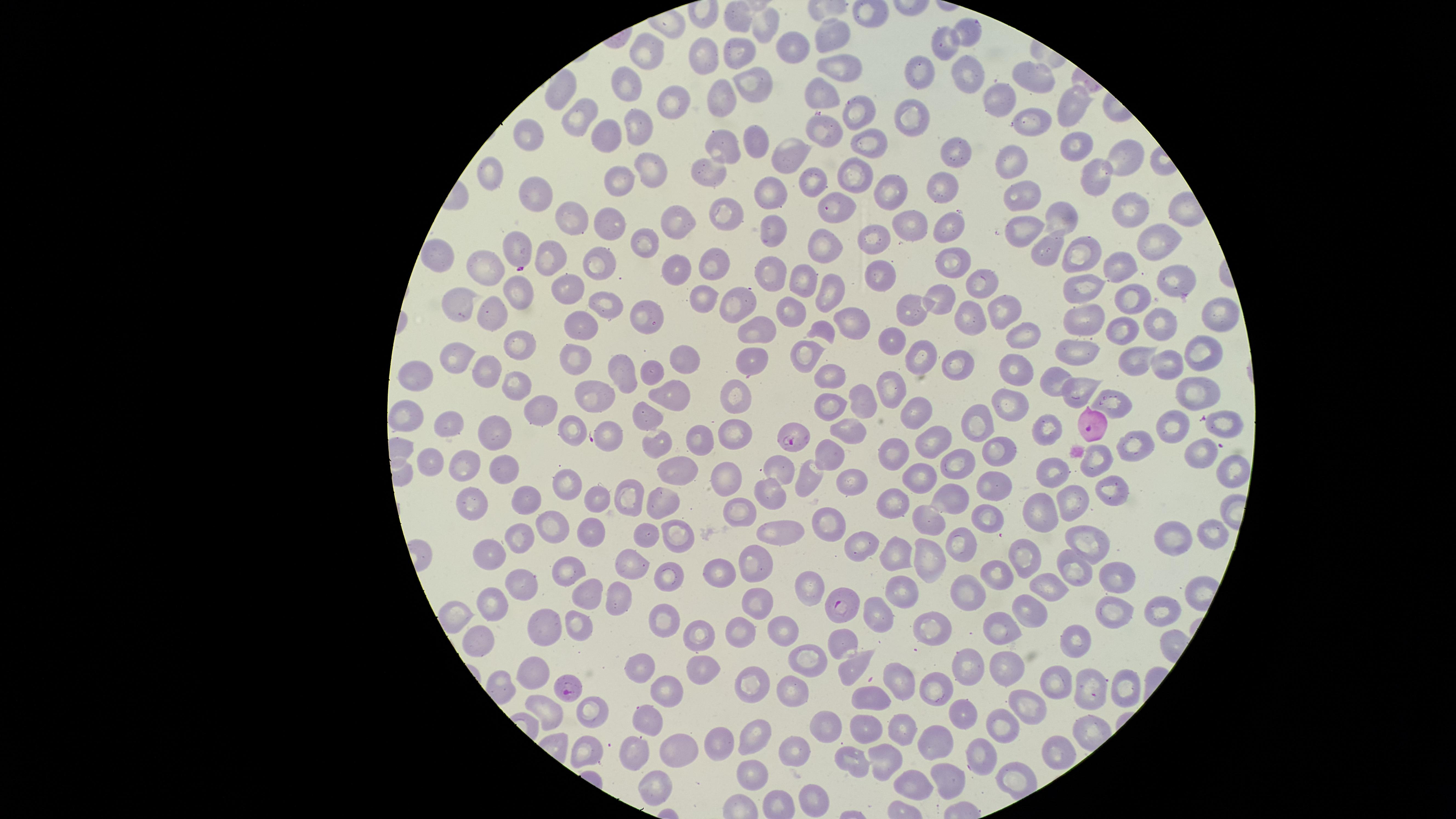

stain = Giemsa
uninfected RBCs = approximate marker points as (x, y) in pixels: (737, 17), (764, 30), (966, 31), (837, 38), (946, 44), (737, 50), (792, 51), (644, 56), (704, 59), (839, 70), (965, 72), (1038, 74), (919, 76), (623, 81), (752, 83), (557, 91), (823, 94), (724, 98), (1002, 99), (671, 105), (1065, 109), (583, 114), (857, 117), (909, 119), (1031, 120), (822, 125), (635, 130), (609, 132), (530, 136), (753, 140), (722, 144), (868, 144), (1071, 147), (790, 149), (951, 152), (1123, 156), (1009, 163), (494, 167), (650, 167), (710, 169), (1097, 173), (857, 176), (621, 178), (814, 183), (945, 185), (890, 190), (764, 191), (540, 196), (1019, 196), (1130, 210), (832, 211), (725, 213), (1059, 217), (677, 220), (610, 221), (574, 223), (914, 224), (948, 224), (770, 226), (1016, 226), (1157, 235), (643, 243), (871, 243), (1044, 246), (513, 250), (821, 250), (1079, 251), (444, 253), (952, 256), (546, 259), (597, 262), (676, 264), (1125, 265), (721, 266), (770, 270), (483, 273), (886, 273), (1170, 279), (802, 280), (1089, 280), (978, 283), (568, 288), (832, 292), (516, 294), (704, 296), (944, 298), (1131, 299), (460, 303), (795, 306), (606, 307), (737, 308), (907, 310), (999, 311), (646, 315), (489, 316), (964, 316), (1216, 316), (1089, 318), (1155, 319), (841, 320), (585, 328), (819, 328), (1112, 328), (754, 331), (1019, 331), (889, 338), (518, 347), (1203, 347), (807, 351), (1085, 353), (456, 355), (685, 359), (577, 360), (1135, 360), (750, 363), (919, 363), (1170, 363), (962, 368), (649, 370), (1015, 370), (622, 371), (486, 373), (416, 375), (832, 377), (1058, 377), (516, 383), (1075, 386), (888, 389), (1196, 390), (596, 395), (676, 395), (735, 397), (865, 400), (1108, 400), (828, 402), (1007, 403), (536, 410), (912, 412), (644, 415), (410, 418), (975, 421), (1228, 423), (453, 424), (1169, 425), (570, 428), (1050, 429), (496, 430), (848, 431), (737, 432), (607, 437), (696, 440), (935, 442), (657, 446), (1143, 448), (996, 449), (899, 452), (1198, 453), (825, 455), (1096, 458), (427, 460), (463, 465), (959, 465), (497, 469), (1233, 470), (1053, 471), (779, 472), (676, 473), (722, 477), (808, 478), (921, 478), (562, 479), (843, 482), (993, 485), (1110, 487), (629, 495), (769, 495), (892, 497), (595, 498), (948, 498), (1077, 499), (471, 503), (521, 503), (658, 504), (1046, 504), (742, 508), (923, 519), (988, 519), (826, 522), (552, 525), (776, 525), (588, 533), (521, 534), (643, 535), (673, 537), (1205, 538), (1175, 539), (961, 542), (1082, 542), (860, 549), (488, 552), (892, 553), (755, 556), (1027, 556), (926, 558), (634, 562), (718, 568), (1068, 568), (565, 574), (998, 576), (668, 577), (1117, 582), (1046, 587), (519, 588), (802, 588), (975, 589), (620, 592), (897, 593), (582, 596), (754, 600), (493, 605), (1030, 607), (1114, 608), (880, 609), (1158, 610), (666, 620), (924, 622), (788, 624), (572, 629), (996, 629), (535, 630), (699, 632), (736, 634), (1077, 637), (844, 639), (478, 643), (804, 658), (853, 663), (964, 663), (640, 666), (1002, 667), (702, 669), (531, 676), (892, 680), (748, 682), (1056, 682), (1091, 687), (1123, 687), (790, 689), (666, 690), (935, 691), (870, 697), (551, 706), (957, 706), (1030, 706), (592, 712), (652, 715), (897, 725), (864, 727), (1003, 729), (826, 733), (723, 740), (749, 742), (675, 744), (931, 744), (1056, 749), (799, 750), (583, 753), (638, 754), (886, 757), (856, 759), (978, 765), (753, 779), (655, 782), (950, 784), (911, 785), (814, 800)
presence = malaria parasites detected
parasitized RBCs = approximate marker points as (x, y) in pixels: (795, 436), (842, 603), (565, 688)
species = Plasmodium falciparum
preparation = thin blood smear
capture = smartphone photograph through the microscope eyepiece
field of view = single
visible region = circular
image size = 1456×819 pixels